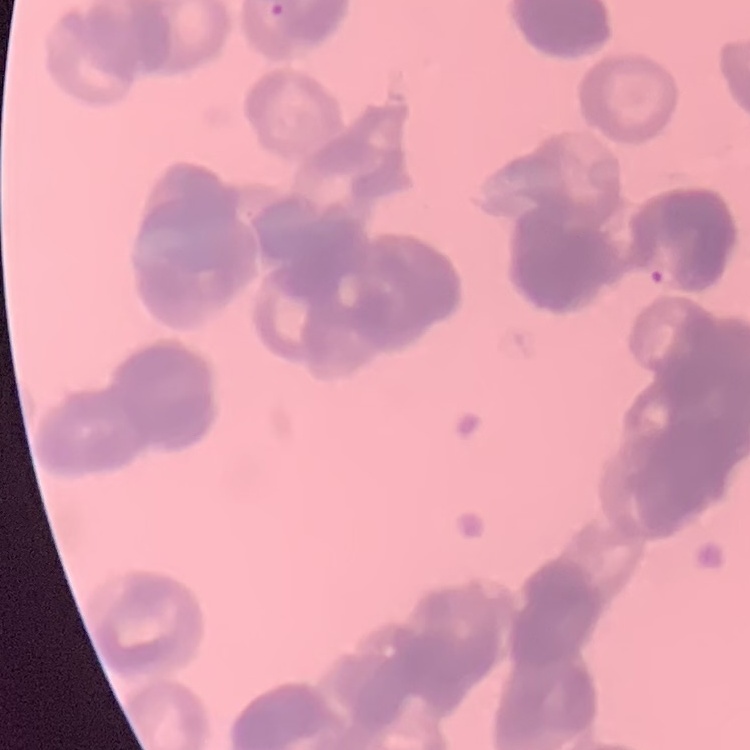
Summary:
  - Red blood cell morphology: rouleaux formation
  - Image type: one tile cut from a larger photomicrograph
  - Preparation: thin peripheral smear
  - Stain: Field's or Giemsa